Point out each Plasmodium parasite.
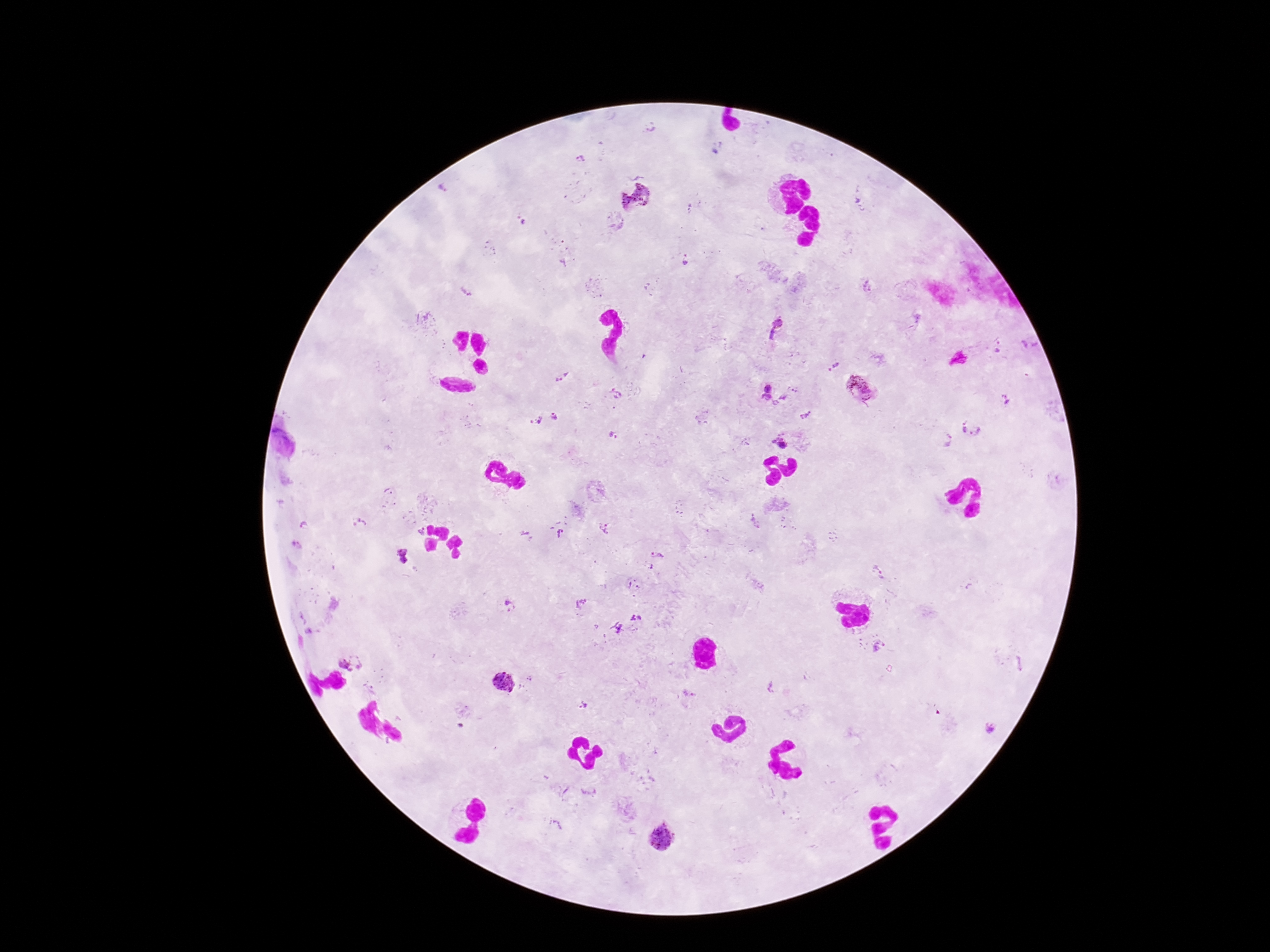

Approximate object centers, in pixels from the top-left corner.
Plasmodium parasites: (x=581, y=159), (x=634, y=196), (x=523, y=223), (x=685, y=260), (x=867, y=286), (x=467, y=291), (x=776, y=330), (x=1028, y=345), (x=1000, y=348), (x=835, y=366), (x=562, y=377), (x=767, y=387), (x=862, y=388), (x=614, y=393), (x=784, y=396), (x=766, y=398), (x=1006, y=400), (x=775, y=403), (x=805, y=415), (x=554, y=417), (x=536, y=420), (x=972, y=425), (x=613, y=436), (x=782, y=438), (x=944, y=438), (x=389, y=492), (x=360, y=524), (x=305, y=525), (x=604, y=529), (x=560, y=533), (x=527, y=535), (x=658, y=554), (x=402, y=557), (x=651, y=567), (x=877, y=573), (x=633, y=585), (x=581, y=604), (x=509, y=607), (x=636, y=619), (x=621, y=630), (x=879, y=647), (x=350, y=663), (x=505, y=682), (x=771, y=686), (x=582, y=705), (x=991, y=726), (x=588, y=793), (x=559, y=825), (x=663, y=837).

Summary:
  - Magnification: 100x
  - Stain: Giemsa
  - Preparation: thick blood film
  - Field of view: one from this slide
  - Image size: 1270×952 pixels
  - Capture: smartphone camera through the microscope eyepiece
  - Patient malaria status: positive